Identify the parasite.
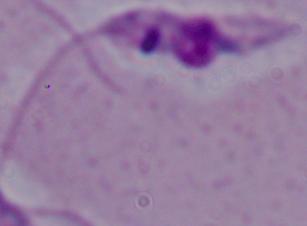

Leishmania.

Summary:
  - Magnification: 1000x
  - Modality: micrograph